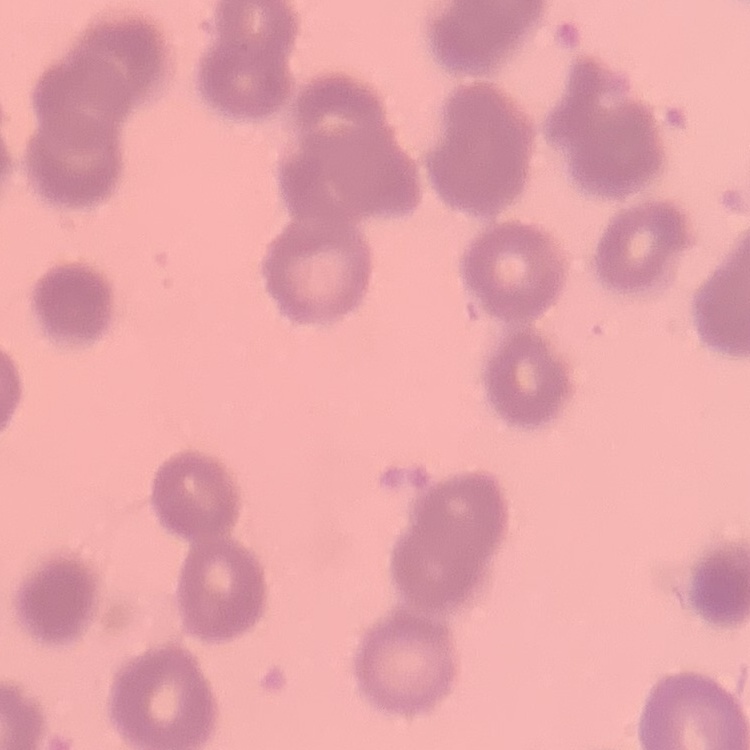
Summary:
  - Erythrocyte morphology: rouleaux formation
  - Preparation: thin blood smear
  - Stain: Field's or Giemsa
  - Image type: one tile cut from a larger photomicrograph